Locate and identify every blood parasite.
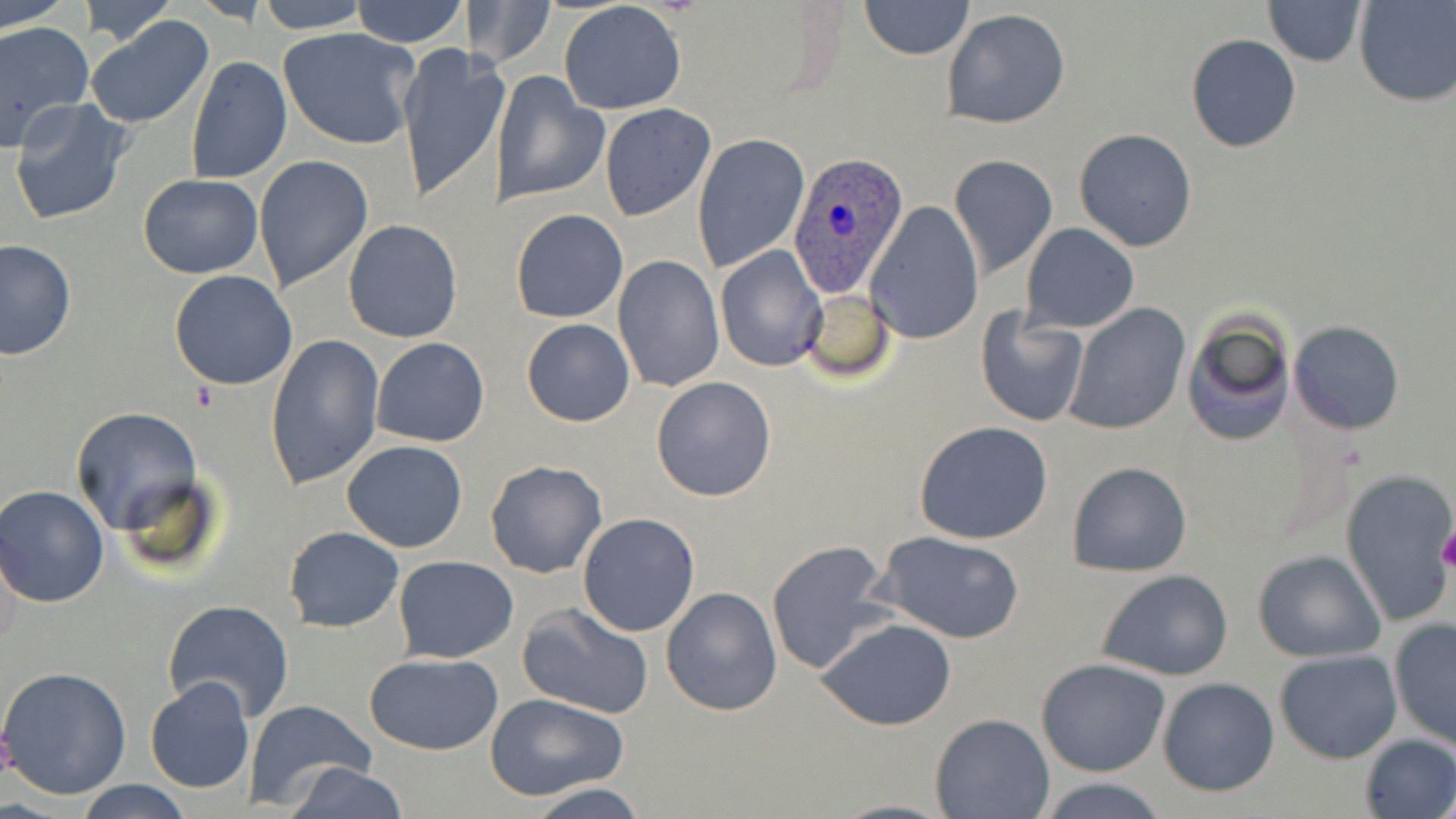
Approximate bounding boxes as named x1/y1/x2/y2 corners in pixels.
Plasmodium ovale-infected red blood cells: (x1=788, y1=153, x2=910, y2=296).
No Plasmodium falciparum, Plasmodium malariae, Plasmodium vivax, Babesia divergens, or Trypanosoma brucei observed.

Summary:
  - Platelet locations: (x1=191, y1=380, x2=221, y2=412), (x1=1438, y1=528, x2=1456, y2=573)
  - Uninfected red blood cell locations: (x1=0, y1=0, x2=71, y2=31), (x1=78, y1=0, x2=177, y2=47), (x1=256, y1=0, x2=369, y2=33), (x1=349, y1=0, x2=467, y2=48), (x1=470, y1=0, x2=556, y2=71), (x1=1262, y1=0, x2=1368, y2=66), (x1=1354, y1=0, x2=1456, y2=106), (x1=558, y1=1, x2=688, y2=115), (x1=859, y1=1, x2=973, y2=60), (x1=942, y1=8, x2=1072, y2=128), (x1=85, y1=15, x2=216, y2=129), (x1=0, y1=20, x2=93, y2=149), (x1=278, y1=27, x2=420, y2=150), (x1=1185, y1=34, x2=1302, y2=152), (x1=396, y1=42, x2=504, y2=206), (x1=187, y1=56, x2=291, y2=183), (x1=492, y1=71, x2=609, y2=206), (x1=9, y1=99, x2=131, y2=224), (x1=599, y1=103, x2=715, y2=220), (x1=1074, y1=128, x2=1199, y2=250), (x1=692, y1=135, x2=810, y2=273), (x1=949, y1=155, x2=1059, y2=279), (x1=255, y1=156, x2=373, y2=292), (x1=137, y1=174, x2=263, y2=279), (x1=867, y1=200, x2=983, y2=343), (x1=512, y1=208, x2=627, y2=323), (x1=342, y1=219, x2=462, y2=343), (x1=1020, y1=223, x2=1140, y2=332), (x1=0, y1=238, x2=76, y2=360), (x1=716, y1=246, x2=826, y2=373), (x1=612, y1=256, x2=723, y2=392), (x1=168, y1=270, x2=297, y2=391), (x1=800, y1=288, x2=897, y2=383), (x1=1063, y1=302, x2=1190, y2=434), (x1=975, y1=309, x2=1089, y2=426), (x1=1182, y1=312, x2=1295, y2=447), (x1=521, y1=318, x2=635, y2=427), (x1=1289, y1=320, x2=1404, y2=433), (x1=265, y1=331, x2=385, y2=493), (x1=372, y1=337, x2=490, y2=447), (x1=651, y1=376, x2=778, y2=502), (x1=70, y1=404, x2=201, y2=540), (x1=914, y1=420, x2=1053, y2=542), (x1=340, y1=440, x2=469, y2=553), (x1=484, y1=458, x2=607, y2=578), (x1=1066, y1=460, x2=1192, y2=577), (x1=1340, y1=468, x2=1456, y2=628), (x1=0, y1=486, x2=112, y2=607), (x1=577, y1=512, x2=700, y2=637), (x1=284, y1=526, x2=404, y2=631), (x1=874, y1=530, x2=1025, y2=642), (x1=765, y1=540, x2=896, y2=676), (x1=1252, y1=550, x2=1386, y2=660), (x1=394, y1=555, x2=518, y2=664), (x1=1097, y1=568, x2=1233, y2=680), (x1=661, y1=586, x2=783, y2=716), (x1=162, y1=599, x2=295, y2=722), (x1=518, y1=600, x2=654, y2=719), (x1=1388, y1=618, x2=1455, y2=750), (x1=818, y1=619, x2=956, y2=731), (x1=1274, y1=648, x2=1402, y2=763), (x1=363, y1=652, x2=505, y2=755), (x1=1037, y1=658, x2=1169, y2=775), (x1=0, y1=665, x2=132, y2=799), (x1=1157, y1=676, x2=1279, y2=796), (x1=144, y1=677, x2=255, y2=794), (x1=486, y1=693, x2=629, y2=801), (x1=243, y1=701, x2=377, y2=811), (x1=930, y1=712, x2=1054, y2=818), (x1=1358, y1=733, x2=1456, y2=818), (x1=281, y1=762, x2=409, y2=819), (x1=1035, y1=778, x2=1172, y2=818), (x1=74, y1=780, x2=193, y2=819), (x1=525, y1=785, x2=650, y2=819)
  - Slide-level diagnosis: Plasmodium ovale
  - Magnification: 1000x
  - Field of view: one of a larger specimen
  - Modality: light microscopy
  - Image size: 1456×819 pixels
  - Stain: May-Grünwald-Giemsa
  - Preparation: thin blood film